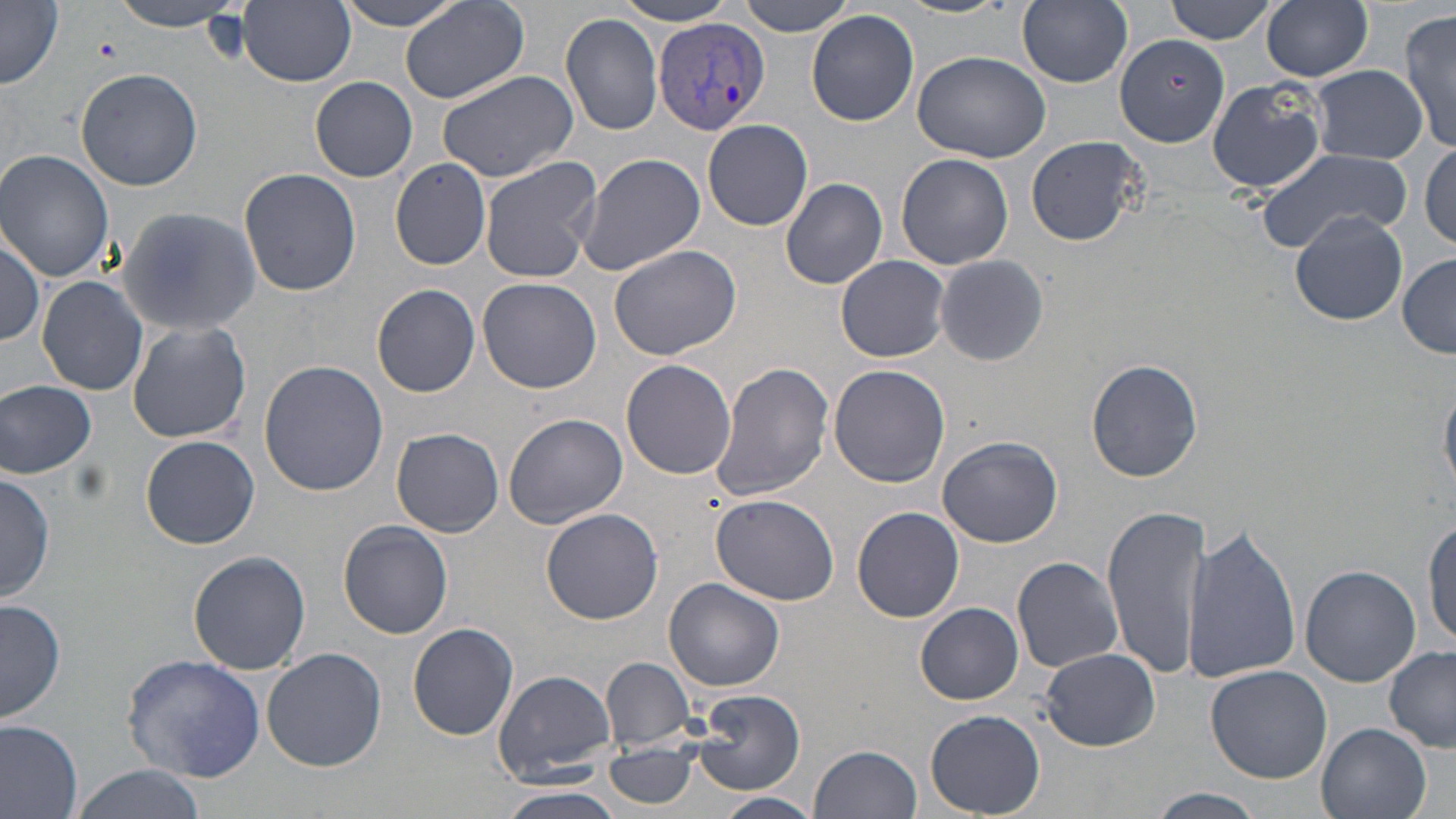

{
  "slide_level_diagnosis": "Plasmodium vivax",
  "image_size": "1456×819 pixels",
  "modality": "optical microscopy",
  "magnification": "1000x",
  "plasmodium_vivax_infected_red_blood_cell_locations": "approximate bounding boxes as (x1, y1, x2, y2) in pixels: (652, 16, 770, 137)",
  "preparation": "thin blood film",
  "stain": "May-Grünwald-Giemsa",
  "field_of_view": "one of a larger specimen",
  "uninfected_red_blood_cell_locations": "approximate bounding boxes as (x1, y1, x2, y2) in pixels: (107, 0, 246, 31), (333, 0, 471, 31), (734, 0, 858, 35), (892, 0, 1017, 18), (1018, 0, 1133, 87), (1164, 0, 1278, 44), (1, 1, 62, 90), (238, 1, 355, 86), (611, 1, 740, 26), (1260, 1, 1374, 81), (401, 2, 531, 104), (1401, 8, 1456, 154), (806, 10, 919, 127), (559, 12, 665, 137), (1115, 33, 1230, 147), (912, 49, 1052, 165), (76, 66, 202, 190), (436, 67, 582, 185), (1311, 67, 1428, 162), (309, 76, 419, 182), (1205, 79, 1330, 194), (398, 89, 543, 227), (703, 119, 813, 231), (1026, 136, 1144, 246), (1419, 144, 1455, 252), (1, 150, 118, 282), (1254, 150, 1415, 253), (576, 153, 704, 277), (896, 154, 1013, 270), (478, 157, 602, 283), (389, 158, 492, 270), (237, 167, 361, 296), (780, 177, 888, 290), (117, 207, 261, 336), (1292, 211, 1407, 325), (0, 228, 45, 348), (609, 244, 741, 360), (933, 253, 1049, 366), (836, 255, 950, 362), (1398, 255, 1456, 357), (36, 276, 149, 395), (476, 277, 602, 393), (372, 283, 480, 397), (127, 320, 252, 444), (1087, 358, 1202, 482), (258, 359, 389, 496), (621, 359, 737, 480), (709, 362, 835, 503), (828, 365, 950, 487), (0, 379, 97, 478), (1440, 381, 1455, 494), (502, 412, 630, 530), (391, 428, 504, 537), (139, 434, 261, 549), (937, 434, 1061, 548), (1, 471, 55, 603), (711, 493, 840, 605), (852, 506, 965, 623), (1104, 506, 1210, 679), (541, 508, 664, 624), (1422, 515, 1456, 651), (338, 520, 452, 639), (1181, 522, 1302, 687), (188, 550, 312, 675), (1013, 555, 1125, 673), (1299, 565, 1420, 685), (663, 578, 784, 691), (1, 597, 67, 721), (916, 603, 1023, 704), (408, 623, 519, 740), (262, 647, 387, 772), (1385, 647, 1456, 751), (1040, 648, 1161, 749), (122, 653, 266, 783), (601, 656, 698, 749), (1205, 665, 1332, 784), (494, 668, 619, 784), (695, 689, 804, 793), (924, 711, 1046, 819), (0, 720, 83, 819), (1317, 723, 1432, 819), (605, 742, 701, 810), (811, 744, 922, 819), (68, 766, 209, 819), (497, 788, 626, 819), (1141, 790, 1270, 819), (716, 792, 821, 819)"
}